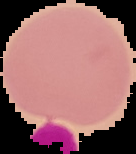 Result: no malaria parasites detected. From a thin blood film. Image is 136×154 pixels. Cell region segmented out of the field of view; the surrounding area is masked to black.